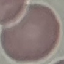

result = no malaria parasites seen
preparation = thin blood film
capture = smartphone through the microscope eyepiece
image type = automatically extracted cell patch, resized to 64 × 64 pixels
stain = Giemsa